Assess this cell for malaria.
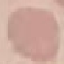

Uninfected.

Thin blood smear. Acquired by smartphone through the microscope eyepiece. Giemsa-stained preparation. Automatically extracted cell patch, resized to 64 × 64 pixels.